Locate and identify every blood parasite.
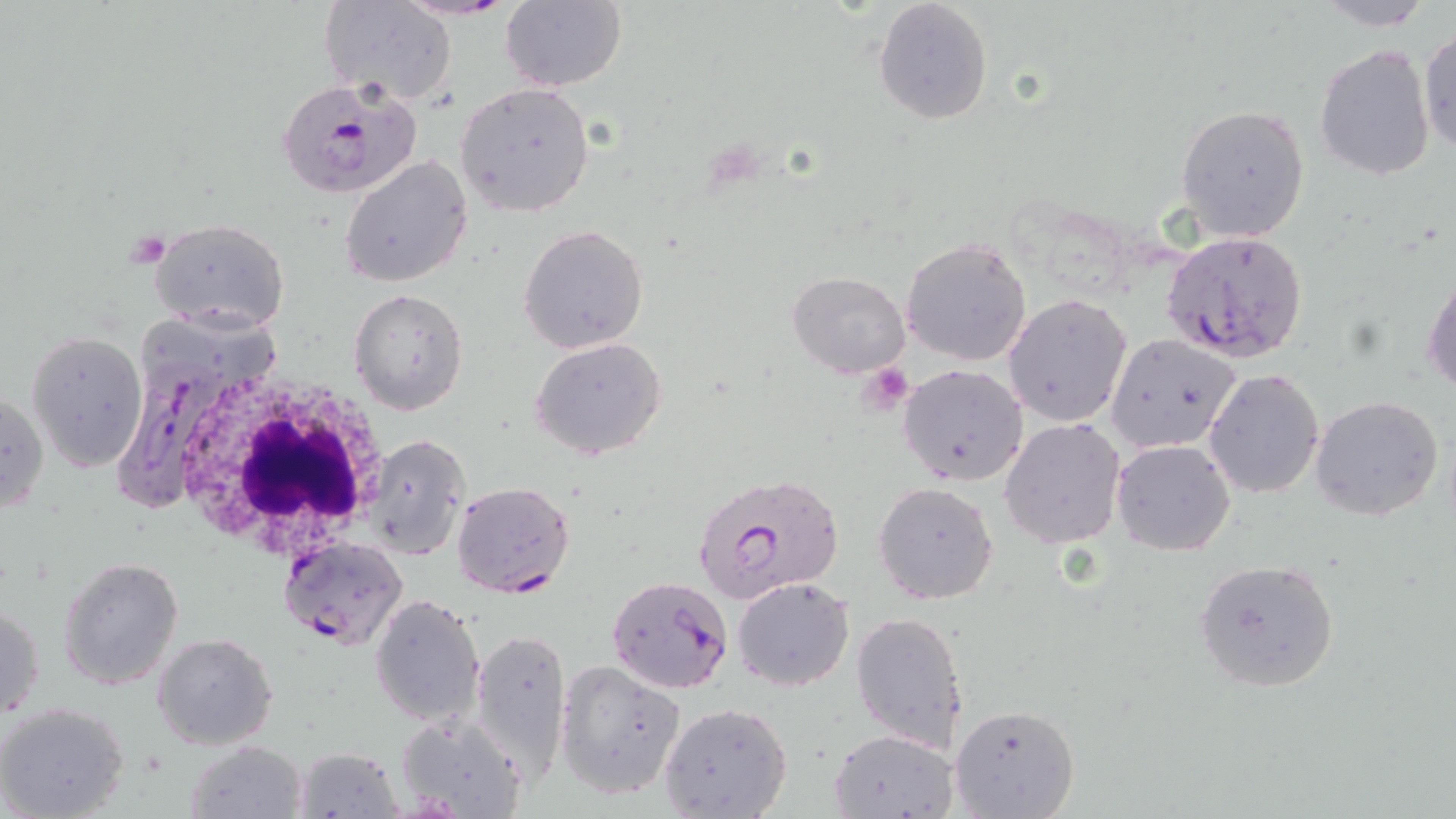
Approximate bounding boxes as [x1, y1, x2, y2] in pixels.
Plasmodium falciparum-infected red blood cells: [396, 0, 519, 20], [278, 82, 420, 197], [1161, 230, 1307, 359], [105, 319, 240, 513], [691, 471, 844, 605], [452, 481, 575, 597], [279, 536, 409, 651], [606, 576, 734, 694].
No Plasmodium ovale, Plasmodium malariae, Plasmodium vivax, Babesia divergens, or Trypanosoma brucei observed.

Uninfected red blood cell locations: [321, 0, 457, 106], [500, 0, 627, 90], [1305, 0, 1444, 28], [872, 1, 994, 124], [1419, 28, 1456, 157], [1313, 43, 1436, 181], [455, 82, 595, 217], [1176, 102, 1313, 242], [340, 156, 474, 287], [147, 216, 291, 335], [519, 224, 649, 354], [901, 237, 1031, 365], [1423, 262, 1455, 400], [788, 271, 911, 377], [348, 287, 468, 415], [1004, 294, 1130, 428], [26, 331, 148, 472], [1107, 333, 1244, 455], [531, 338, 667, 461], [898, 362, 1028, 487], [1205, 369, 1324, 497], [0, 388, 48, 515], [1310, 395, 1444, 522], [1000, 417, 1126, 548], [364, 436, 468, 562], [1112, 439, 1235, 554], [874, 482, 999, 603], [57, 556, 183, 690], [1194, 558, 1339, 692], [732, 577, 855, 691], [370, 593, 486, 727], [1, 601, 45, 722], [850, 609, 969, 752], [470, 628, 572, 781], [152, 632, 277, 750], [553, 659, 687, 800], [0, 701, 131, 819], [658, 701, 793, 818], [948, 703, 1080, 819], [394, 711, 527, 819], [829, 728, 957, 818], [187, 740, 307, 818], [293, 745, 405, 819]. Platelet locations: [127, 229, 171, 267], [860, 364, 916, 413]. White blood cell locations: [169, 370, 388, 557]. Slide-level diagnosis: Plasmodium falciparum. May-Grünwald-Giemsa-stained preparation. Thin blood film. Image is 1456×819 pixels. Captured at 1000x magnification. Light microscopy. Single field of view.